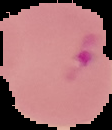
Summary:
  - Preparation: thin blood film
  - Image size: 112×130 pixels
  - Result: malaria parasites identified
  - Image type: segmented cell region on a black background